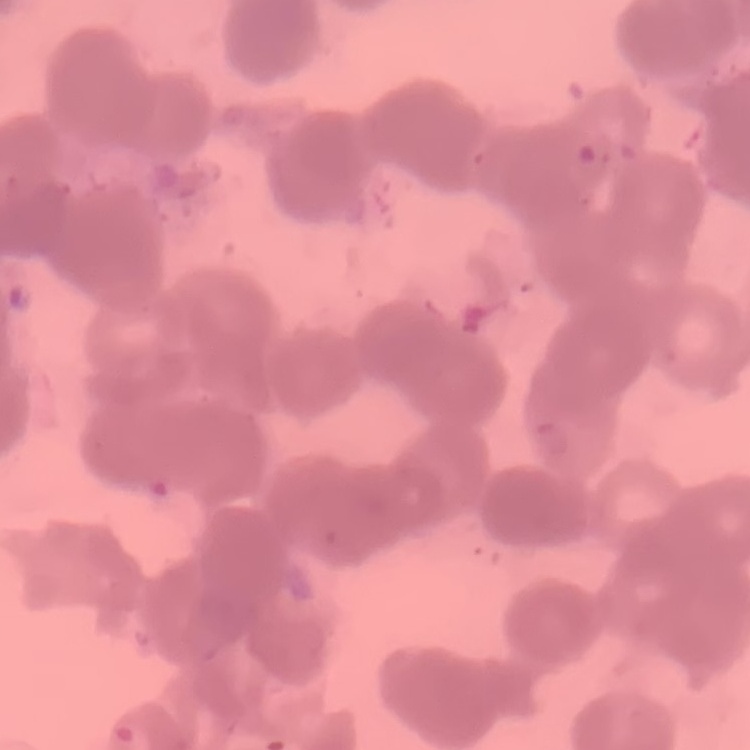

erythrocyte morphology = rouleaux formation
stain = Field's or Giemsa
image type = one tile cut from a larger photomicrograph
preparation = thin blood smear